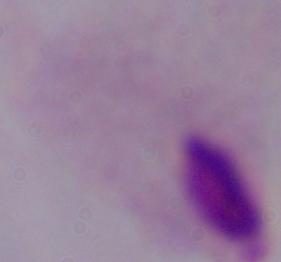

Summary:
  - Identification: trichomonad
  - Magnification: 1000x
  - Modality: photomicrograph